Give the position of every leukocyte visible.
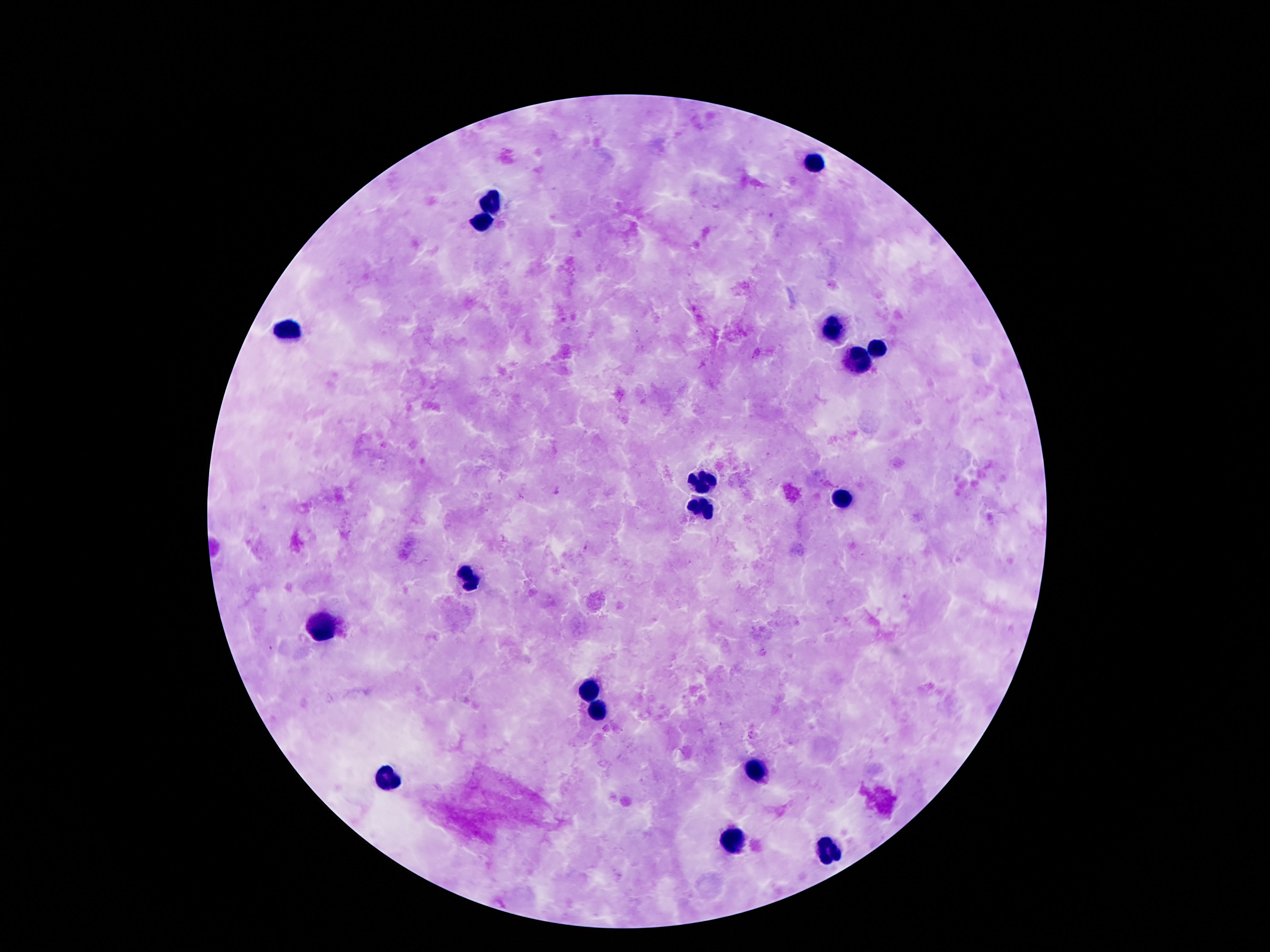
Approximate centers as (x, y) in pixels.
Leukocytes: (814, 163), (489, 199), (480, 221), (829, 326), (288, 330), (878, 349), (857, 361), (700, 480), (843, 500), (698, 507), (466, 582), (325, 631), (591, 688), (599, 713), (757, 770), (386, 781), (732, 842), (828, 851).

Summary:
  - Field of view: one from this slide
  - Patient malaria status: uninfected
  - Image size: 1270×952 pixels
  - Preparation: thick blood film
  - Capture: smartphone camera through the microscope eyepiece
  - Stain: Giemsa
  - Magnification: 100x